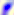
Summary:
  - Magnification: 400x
  - Identification: Toxoplasma gondii
  - Modality: photomicrograph